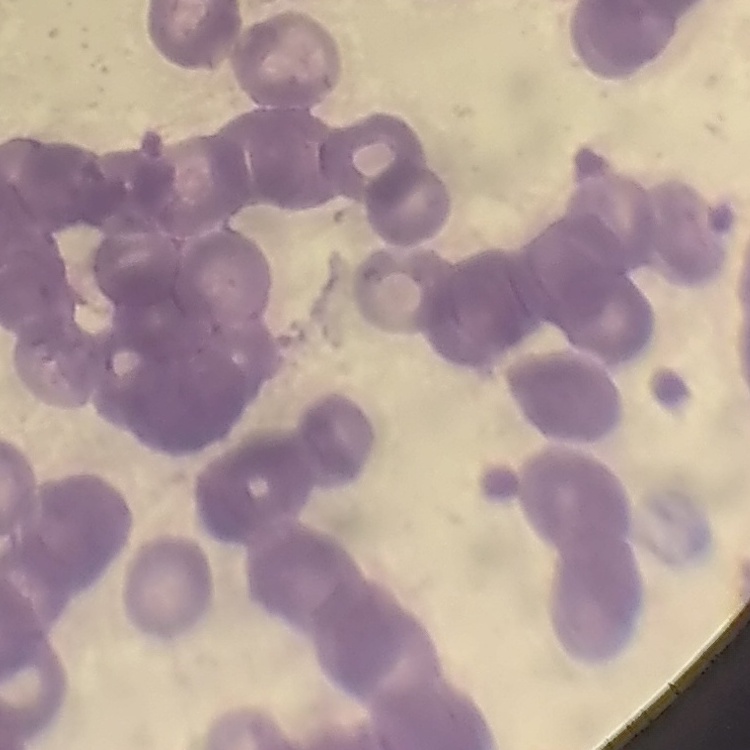

red blood cell morphology = rouleaux formation
preparation = thin blood smear
image type = square crop of a larger photomicrograph
stain = Field's or Giemsa